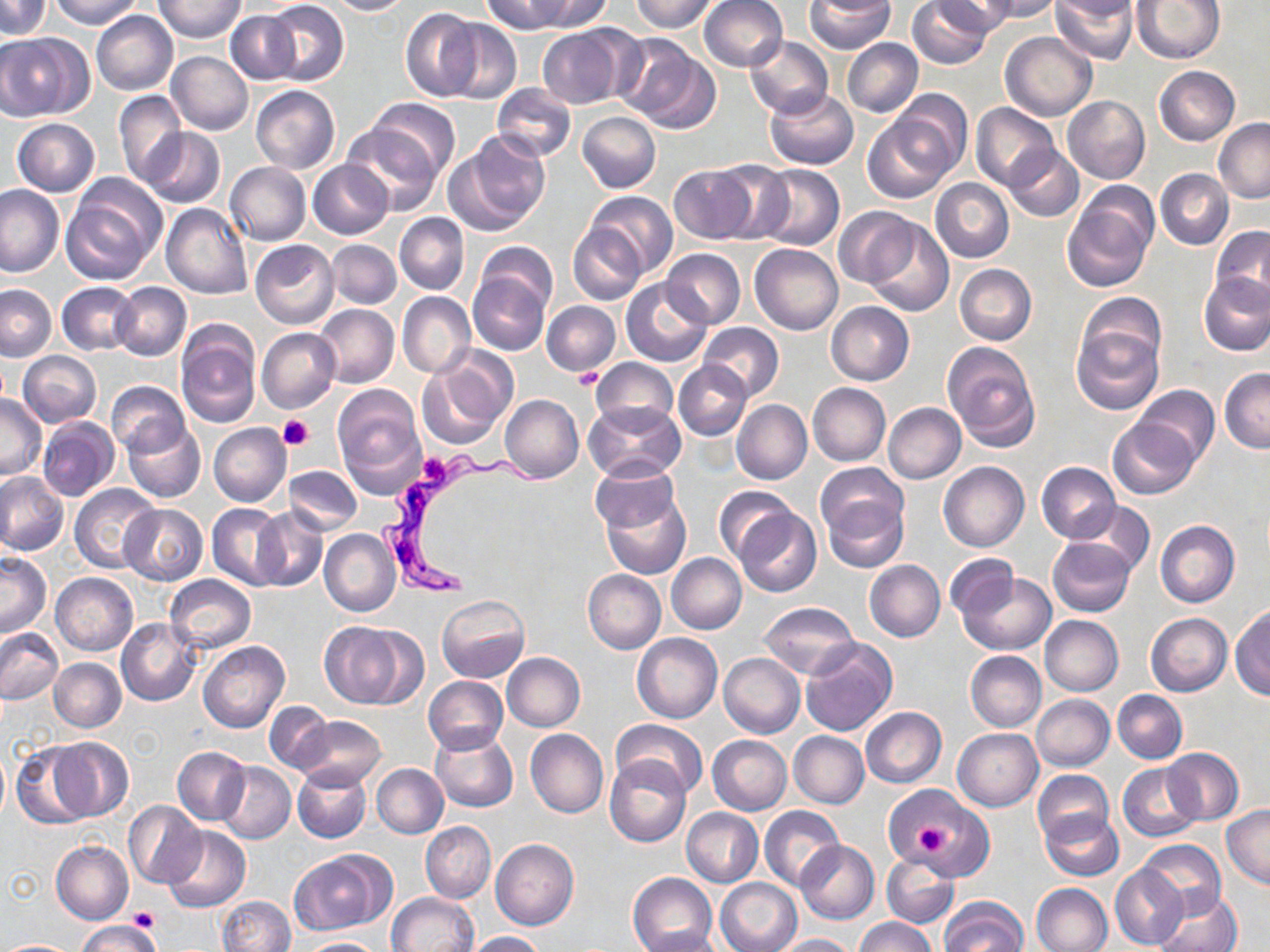
Approximate bounding boxes as named x1/y1/x2/y2 corners in pixels. Platelet locations: (x1=568, y1=369, x2=606, y2=390), (x1=279, y1=414, x2=314, y2=451), (x1=414, y1=453, x2=457, y2=490), (x1=914, y1=819, x2=958, y2=861), (x1=128, y1=907, x2=159, y2=931). Trypanosoma brucei locations: (x1=377, y1=451, x2=552, y2=603). Uninfected red blood cell locations: (x1=0, y1=0, x2=50, y2=39), (x1=48, y1=0, x2=145, y2=27), (x1=155, y1=0, x2=244, y2=43), (x1=324, y1=0, x2=412, y2=15), (x1=482, y1=0, x2=572, y2=35), (x1=526, y1=0, x2=611, y2=32), (x1=629, y1=0, x2=718, y2=33), (x1=699, y1=0, x2=787, y2=72), (x1=907, y1=0, x2=993, y2=69), (x1=929, y1=0, x2=1015, y2=38), (x1=980, y1=0, x2=1061, y2=22), (x1=1051, y1=0, x2=1138, y2=64), (x1=1133, y1=0, x2=1223, y2=63), (x1=265, y1=1, x2=349, y2=86), (x1=805, y1=1, x2=895, y2=53), (x1=1051, y1=1, x2=1137, y2=22), (x1=401, y1=8, x2=481, y2=101), (x1=226, y1=10, x2=301, y2=84), (x1=91, y1=11, x2=178, y2=96), (x1=439, y1=18, x2=522, y2=105), (x1=536, y1=25, x2=635, y2=108), (x1=1000, y1=31, x2=1097, y2=121), (x1=0, y1=33, x2=86, y2=121), (x1=614, y1=35, x2=719, y2=133), (x1=744, y1=35, x2=833, y2=119), (x1=842, y1=38, x2=923, y2=117), (x1=167, y1=51, x2=253, y2=135), (x1=1153, y1=66, x2=1240, y2=146), (x1=492, y1=84, x2=576, y2=161), (x1=251, y1=86, x2=340, y2=174), (x1=765, y1=87, x2=858, y2=169), (x1=886, y1=89, x2=972, y2=177), (x1=113, y1=90, x2=186, y2=185), (x1=1062, y1=95, x2=1150, y2=183), (x1=366, y1=98, x2=460, y2=178), (x1=971, y1=103, x2=1060, y2=190), (x1=577, y1=111, x2=661, y2=193), (x1=864, y1=114, x2=955, y2=202), (x1=12, y1=118, x2=99, y2=196), (x1=1213, y1=119, x2=1270, y2=204), (x1=342, y1=120, x2=444, y2=216), (x1=141, y1=127, x2=225, y2=208), (x1=449, y1=130, x2=552, y2=234), (x1=1004, y1=145, x2=1084, y2=222), (x1=308, y1=159, x2=394, y2=239), (x1=710, y1=161, x2=794, y2=244), (x1=224, y1=162, x2=311, y2=245), (x1=668, y1=164, x2=756, y2=245), (x1=754, y1=164, x2=845, y2=251), (x1=1156, y1=169, x2=1233, y2=250), (x1=61, y1=177, x2=165, y2=284), (x1=931, y1=177, x2=1014, y2=263), (x1=0, y1=186, x2=66, y2=277), (x1=1063, y1=190, x2=1156, y2=292), (x1=586, y1=191, x2=678, y2=275), (x1=161, y1=203, x2=253, y2=298), (x1=833, y1=207, x2=920, y2=288), (x1=394, y1=212, x2=469, y2=294), (x1=864, y1=219, x2=953, y2=318), (x1=568, y1=223, x2=648, y2=305), (x1=1210, y1=226, x2=1270, y2=305), (x1=250, y1=238, x2=339, y2=329), (x1=327, y1=239, x2=401, y2=309), (x1=476, y1=243, x2=557, y2=318), (x1=750, y1=243, x2=843, y2=335), (x1=662, y1=249, x2=745, y2=328), (x1=955, y1=264, x2=1037, y2=344), (x1=468, y1=268, x2=553, y2=357), (x1=1199, y1=273, x2=1270, y2=356), (x1=622, y1=279, x2=712, y2=366), (x1=57, y1=281, x2=138, y2=355), (x1=111, y1=282, x2=191, y2=359), (x1=0, y1=284, x2=55, y2=361), (x1=397, y1=292, x2=475, y2=378), (x1=1075, y1=294, x2=1166, y2=378), (x1=541, y1=301, x2=621, y2=374), (x1=825, y1=302, x2=914, y2=385), (x1=314, y1=304, x2=400, y2=388), (x1=698, y1=322, x2=783, y2=402), (x1=1070, y1=323, x2=1164, y2=415), (x1=176, y1=324, x2=261, y2=427), (x1=256, y1=327, x2=340, y2=413), (x1=942, y1=341, x2=1041, y2=450), (x1=19, y1=352, x2=101, y2=426), (x1=418, y1=357, x2=511, y2=449), (x1=591, y1=358, x2=678, y2=431), (x1=673, y1=361, x2=751, y2=440), (x1=1219, y1=368, x2=1270, y2=452), (x1=106, y1=381, x2=189, y2=456), (x1=808, y1=383, x2=891, y2=466), (x1=1134, y1=385, x2=1219, y2=465), (x1=332, y1=386, x2=425, y2=494), (x1=0, y1=391, x2=46, y2=479), (x1=733, y1=393, x2=886, y2=472), (x1=500, y1=395, x2=584, y2=483), (x1=732, y1=399, x2=812, y2=484), (x1=584, y1=401, x2=686, y2=483), (x1=883, y1=402, x2=966, y2=483), (x1=38, y1=416, x2=119, y2=501), (x1=1108, y1=417, x2=1201, y2=499), (x1=122, y1=418, x2=205, y2=503), (x1=209, y1=423, x2=291, y2=507), (x1=939, y1=461, x2=1029, y2=551), (x1=590, y1=462, x2=680, y2=534), (x1=1036, y1=462, x2=1121, y2=544), (x1=815, y1=463, x2=907, y2=541), (x1=284, y1=466, x2=362, y2=534), (x1=0, y1=471, x2=68, y2=556), (x1=70, y1=483, x2=162, y2=574), (x1=600, y1=486, x2=691, y2=580), (x1=714, y1=487, x2=797, y2=565), (x1=822, y1=488, x2=909, y2=573), (x1=1072, y1=501, x2=1154, y2=576), (x1=120, y1=504, x2=207, y2=585), (x1=207, y1=504, x2=287, y2=589), (x1=735, y1=506, x2=821, y2=597), (x1=252, y1=508, x2=328, y2=592), (x1=1154, y1=520, x2=1239, y2=607), (x1=320, y1=529, x2=401, y2=617), (x1=1047, y1=537, x2=1137, y2=617), (x1=0, y1=553, x2=51, y2=637), (x1=666, y1=553, x2=747, y2=634), (x1=944, y1=554, x2=1016, y2=619), (x1=865, y1=559, x2=944, y2=642), (x1=583, y1=569, x2=666, y2=653), (x1=958, y1=571, x2=1057, y2=655), (x1=51, y1=572, x2=138, y2=655), (x1=165, y1=574, x2=256, y2=654), (x1=437, y1=594, x2=529, y2=683), (x1=759, y1=601, x2=860, y2=679), (x1=1231, y1=607, x2=1270, y2=700), (x1=1145, y1=613, x2=1232, y2=696), (x1=1040, y1=615, x2=1124, y2=695), (x1=117, y1=617, x2=201, y2=706), (x1=320, y1=621, x2=418, y2=709), (x1=0, y1=629, x2=64, y2=704), (x1=632, y1=633, x2=722, y2=723), (x1=800, y1=638, x2=897, y2=737), (x1=199, y1=641, x2=289, y2=734), (x1=965, y1=651, x2=1046, y2=732), (x1=502, y1=652, x2=585, y2=731), (x1=719, y1=652, x2=805, y2=738), (x1=50, y1=658, x2=127, y2=732), (x1=423, y1=675, x2=508, y2=754), (x1=1113, y1=690, x2=1187, y2=763), (x1=1031, y1=694, x2=1115, y2=771), (x1=265, y1=703, x2=335, y2=774), (x1=861, y1=707, x2=946, y2=787), (x1=291, y1=715, x2=385, y2=790), (x1=611, y1=720, x2=709, y2=800), (x1=952, y1=728, x2=1043, y2=810), (x1=526, y1=729, x2=608, y2=818), (x1=429, y1=730, x2=517, y2=812), (x1=789, y1=731, x2=869, y2=808), (x1=708, y1=735, x2=792, y2=814), (x1=48, y1=738, x2=133, y2=821), (x1=10, y1=742, x2=97, y2=829), (x1=172, y1=746, x2=250, y2=825), (x1=0, y1=748, x2=10, y2=821), (x1=1161, y1=748, x2=1244, y2=825), (x1=604, y1=756, x2=690, y2=845), (x1=217, y1=762, x2=296, y2=844), (x1=292, y1=763, x2=371, y2=844), (x1=1118, y1=763, x2=1205, y2=843), (x1=372, y1=764, x2=448, y2=838), (x1=1032, y1=770, x2=1114, y2=848), (x1=892, y1=785, x2=990, y2=878), (x1=123, y1=801, x2=206, y2=889), (x1=1222, y1=805, x2=1270, y2=889), (x1=760, y1=806, x2=845, y2=889), (x1=681, y1=807, x2=762, y2=887), (x1=1040, y1=810, x2=1123, y2=880), (x1=420, y1=822, x2=494, y2=902), (x1=162, y1=824, x2=249, y2=913), (x1=491, y1=839, x2=579, y2=930), (x1=1137, y1=839, x2=1226, y2=919), (x1=794, y1=840, x2=879, y2=924), (x1=51, y1=841, x2=133, y2=924), (x1=289, y1=852, x2=389, y2=934), (x1=882, y1=852, x2=960, y2=927), (x1=1110, y1=864, x2=1188, y2=949), (x1=627, y1=872, x2=718, y2=952), (x1=715, y1=878, x2=801, y2=952), (x1=1030, y1=883, x2=1112, y2=952), (x1=1153, y1=888, x2=1244, y2=952), (x1=387, y1=892, x2=478, y2=952), (x1=217, y1=896, x2=295, y2=952), (x1=939, y1=898, x2=1027, y2=952), (x1=854, y1=916, x2=937, y2=952), (x1=76, y1=921, x2=162, y2=952), (x1=634, y1=928, x2=728, y2=952), (x1=464, y1=931, x2=546, y2=951), (x1=775, y1=934, x2=856, y2=952), (x1=296, y1=937, x2=386, y2=952), (x1=3, y1=940, x2=75, y2=951). Slide-level diagnosis: Trypanosoma brucei. Optical microscopy. Thin blood smear. Image is 1270×952 pixels. 1000x magnification. May-Grünwald-Giemsa-stained preparation. Single field of view.